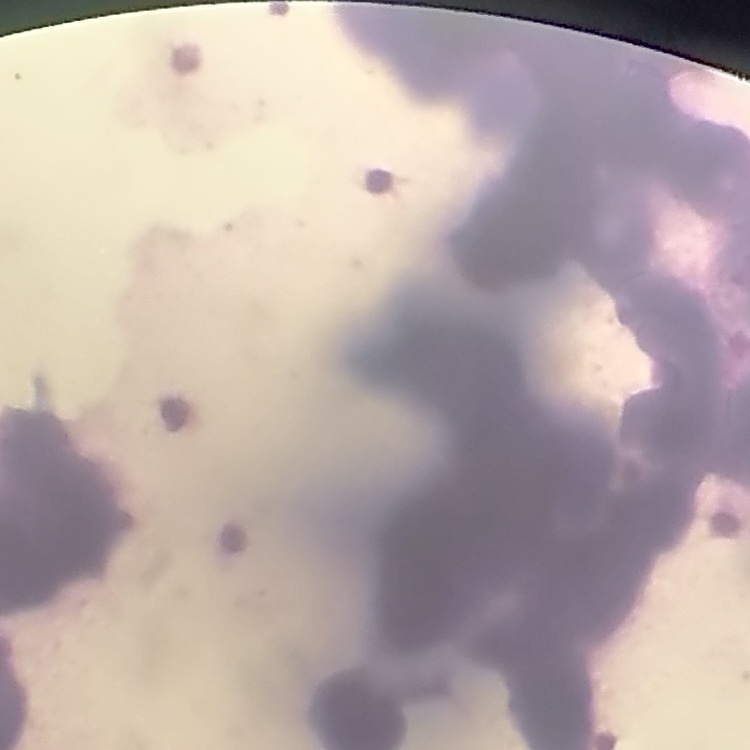
Summary:
  - Erythrocyte morphology: rouleaux formation
  - Stain: Field's or Giemsa
  - Image type: one tile cut from a larger photomicrograph
  - Preparation: thin blood smear